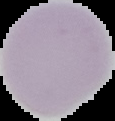
From a thin blood film. Image is 115×121 pixels. Result: no Plasmodium parasites detected. Segmented cell region on a black background.